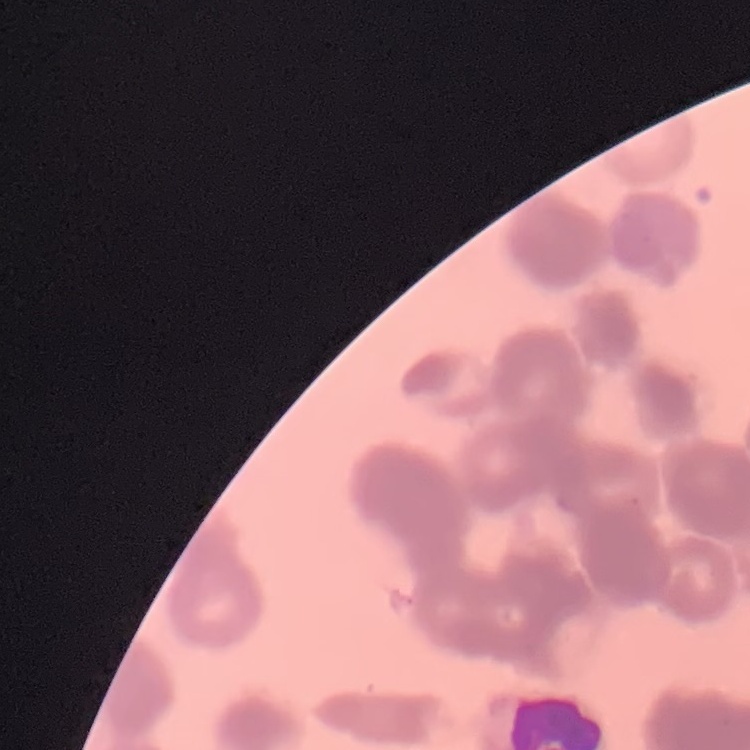

{
  "erythrocyte_morphology": "rouleaux formation",
  "preparation": "thin blood film",
  "image_type": "square crop of a larger photomicrograph",
  "stain": "Field's or Giemsa"
}